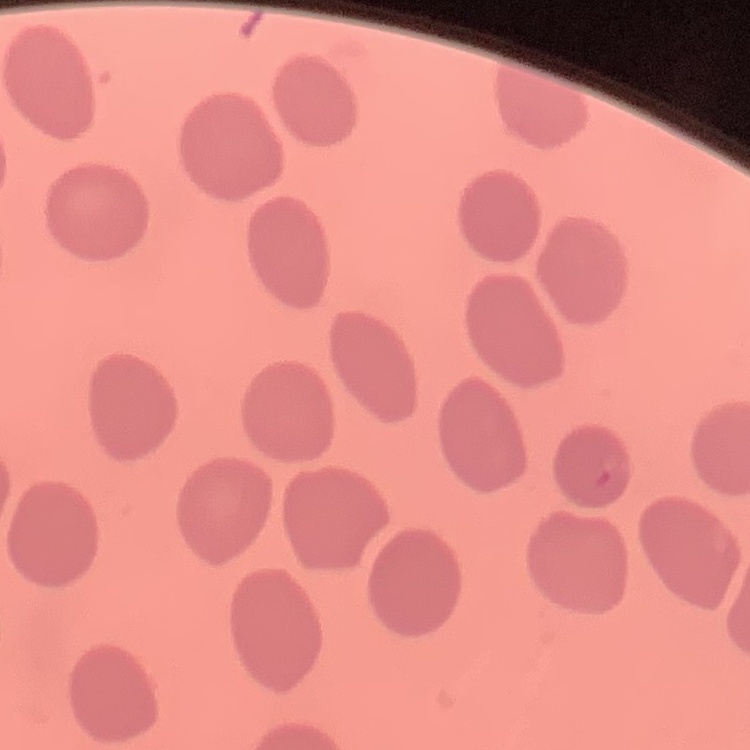
erythrocyte_morphology: no rouleaux formation
preparation: thin blood film
image_type: one tile cut from a larger photomicrograph
stain: Field's or Giemsa